Point out each Plasmodium parasite.
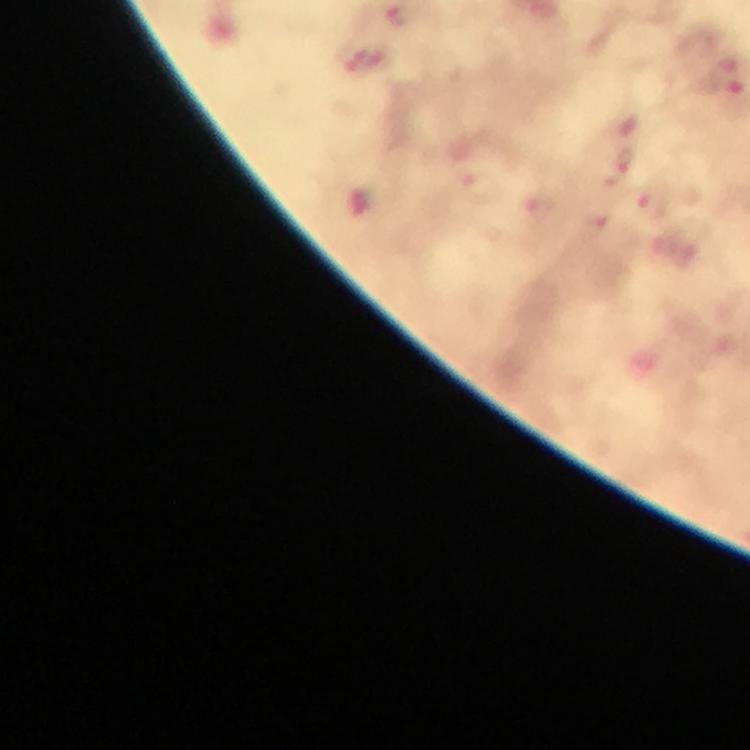

Approximate centers as {x, y} in pixels.
Plasmodium parasites: {397, 14}, {622, 159}, {478, 184}, {539, 206}, {596, 212}.

At 100x magnification. From a malaria diagnostic workup. Photographed with a smartphone mounted on the microscope. Cropped region of a single field of view. Immersion oil applied. Image is 750×750 pixels. Thick smear. Giemsa-stained preparation.